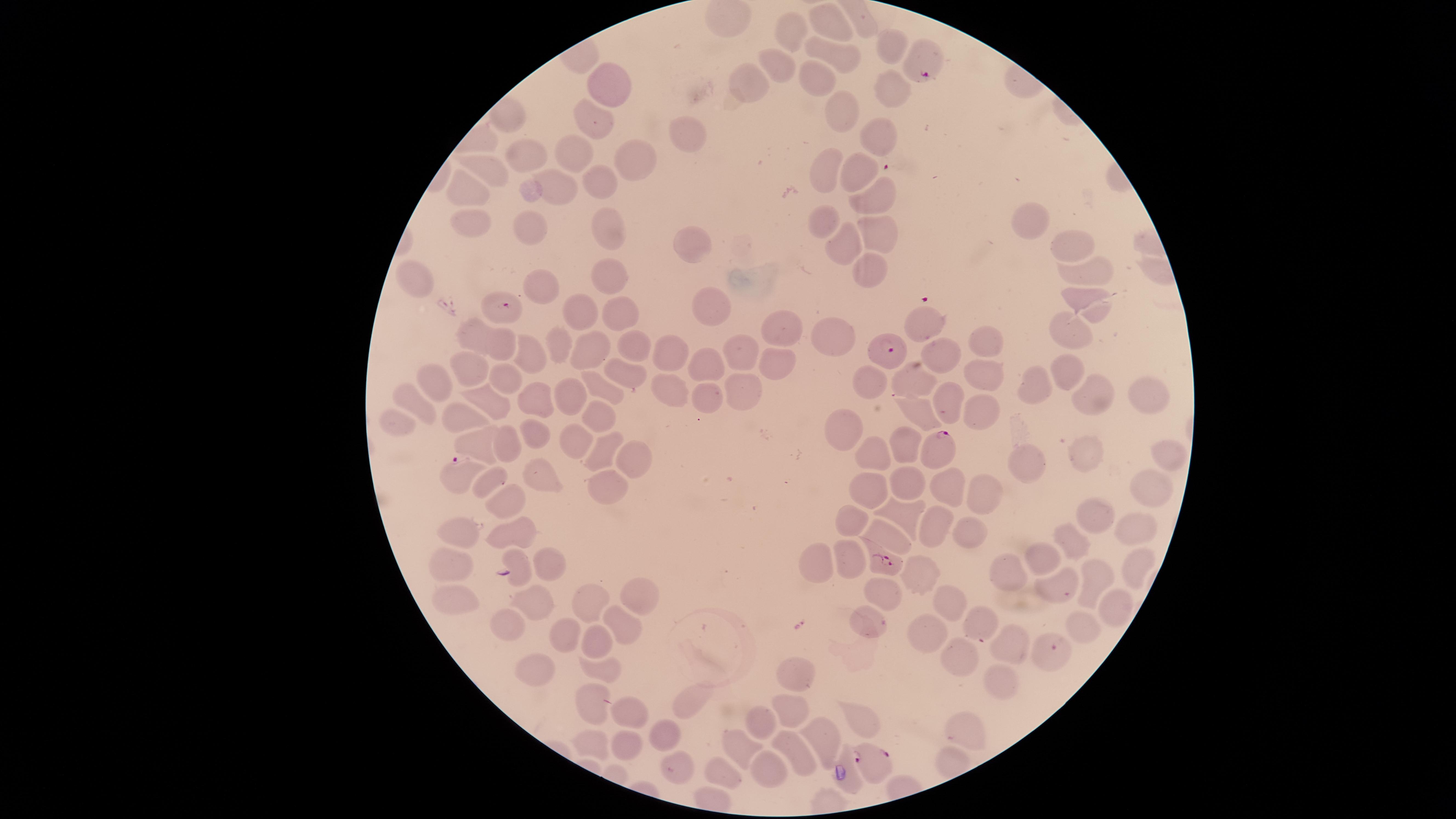
Approximate marker points as [x, y] in pixels.
Summary:
  - Parasitized red blood cells: [927, 76], [501, 306], [886, 347], [940, 445], [456, 462], [884, 559], [1055, 647], [875, 761]
  - Uninfected red blood cells: [829, 24], [785, 34], [887, 46], [829, 53], [776, 65], [815, 78], [611, 82], [749, 86], [891, 92], [841, 120], [594, 123], [687, 129], [879, 135], [526, 155], [576, 155], [634, 155], [857, 168], [488, 169], [827, 170], [603, 181], [467, 190], [563, 191], [879, 200], [835, 223], [879, 223], [466, 225], [608, 225], [1027, 225], [525, 230], [691, 235], [849, 242], [1071, 244], [870, 266], [1087, 267], [609, 273], [412, 281], [541, 286], [1084, 300], [709, 303], [576, 311], [618, 311], [926, 323], [780, 327], [1072, 331], [472, 334], [833, 334], [561, 340], [503, 345], [634, 345], [986, 346], [592, 347], [736, 349], [528, 352], [942, 356], [667, 357], [780, 359], [710, 364], [473, 367], [1061, 367], [988, 372], [623, 373], [511, 376], [436, 377], [918, 378], [605, 384], [868, 384], [747, 390], [410, 392], [566, 392], [1146, 392], [661, 393], [711, 393], [1034, 395], [1092, 396], [486, 397], [536, 401], [946, 404], [986, 408], [595, 414], [924, 415], [461, 419], [396, 422], [529, 429], [851, 429], [576, 442], [904, 444], [477, 445], [506, 450], [604, 452], [1089, 455], [1162, 455], [875, 456], [629, 458], [1027, 459], [535, 471], [494, 480], [868, 483], [907, 484], [606, 488], [944, 488], [1142, 492], [981, 497], [512, 503], [901, 515], [852, 516], [1094, 517], [931, 527], [467, 528], [517, 528], [888, 531], [962, 532], [1132, 536], [1073, 540], [1037, 551], [848, 559], [514, 560], [824, 560], [544, 563], [1013, 564], [455, 565], [918, 568], [1130, 570], [1094, 575], [1062, 586], [883, 588], [638, 590], [590, 597], [536, 598], [944, 605], [457, 607], [1114, 608], [509, 618], [622, 618], [867, 621], [982, 621], [1081, 623], [565, 631], [922, 637], [599, 643], [1014, 643], [957, 658], [533, 669], [604, 669], [795, 669], [997, 683], [590, 697], [686, 701], [793, 704], [631, 710], [864, 717], [763, 721], [966, 729], [668, 732], [823, 732], [591, 744], [626, 746], [796, 746], [739, 751], [679, 768], [773, 768], [724, 771]
  - Visible region: circular
  - Preparation: thin blood film
  - Species: Plasmodium falciparum
  - Presence: malaria parasites seen
  - Field of view: single
  - Capture: smartphone photograph through the microscope eyepiece
  - Image size: 1456×819 pixels
  - Stain: Giemsa